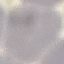 Result: negative for malaria parasites. Automatically extracted cell patch, resized to 64 × 64 pixels. Giemsa stain. Thin smear of blood. Acquired by smartphone through the microscope eyepiece.